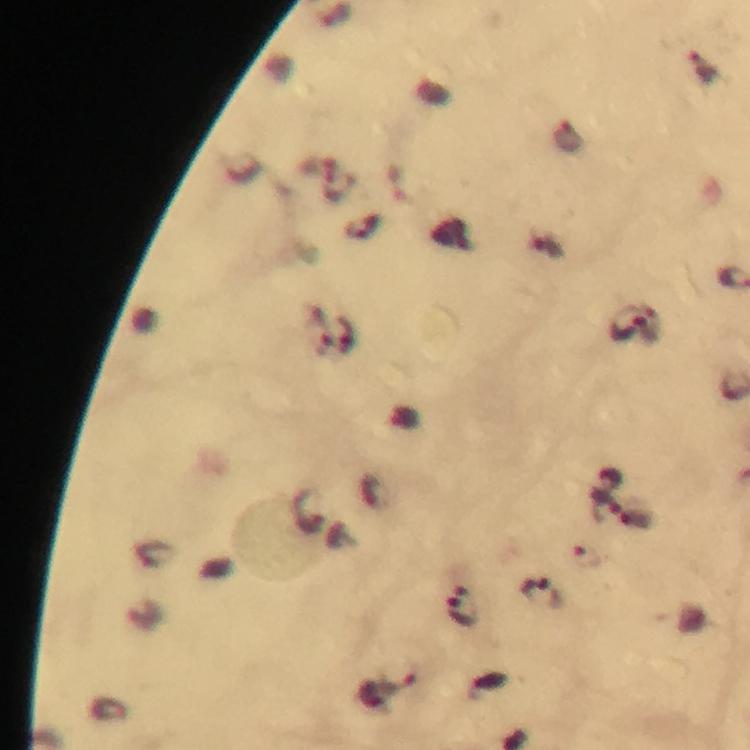
Approximate object centers, in pixels from the top-left corner. Plasmodium parasite locations: (x=705, y=68), (x=339, y=187), (x=627, y=326), (x=319, y=332), (x=307, y=507), (x=609, y=508), (x=587, y=556), (x=543, y=591), (x=464, y=604), (x=383, y=688). From a diagnostic examination for malaria. Immersion oil was used. Cropped region of a single field of view. Thick blood film. Giemsa-stained preparation. Image is 750×750 pixels. Photographed with a smartphone mounted on the microscope. 100x magnification.